Describe the morphology of the red blood cells.
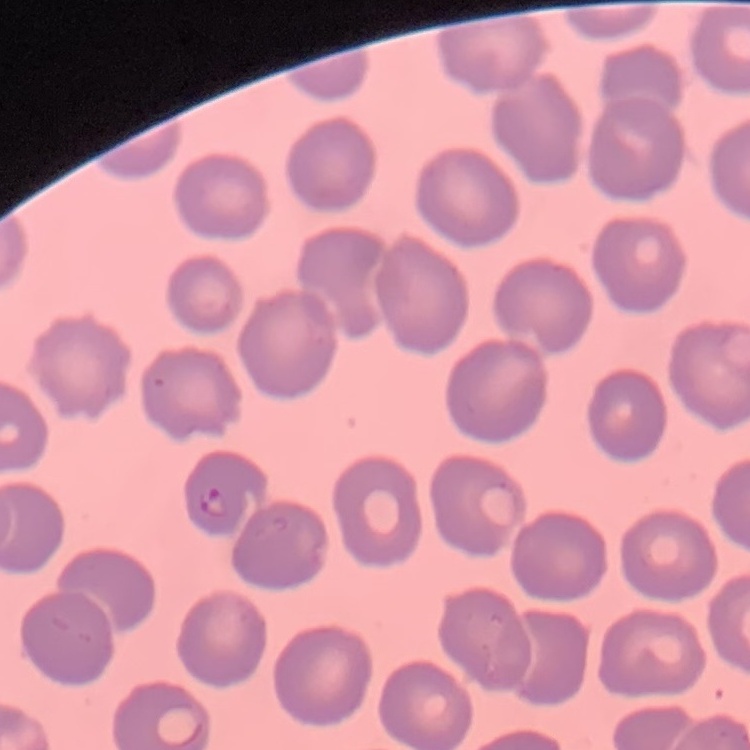
They show no rouleaux formation.

Thin blood film. Field's or Giemsa stain. Square crop of a larger photomicrograph.